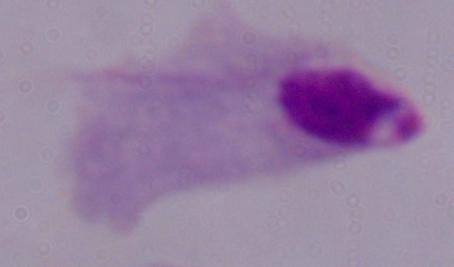

Summary:
  - Modality: micrograph
  - Identification: trichomonad
  - Magnification: 1000x